Classify this cell by malaria status.
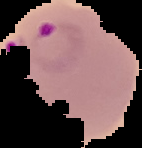
It is parasitized.

image size = 142×148 pixels
preparation = thin blood film
image type = segmented cell region on a black background